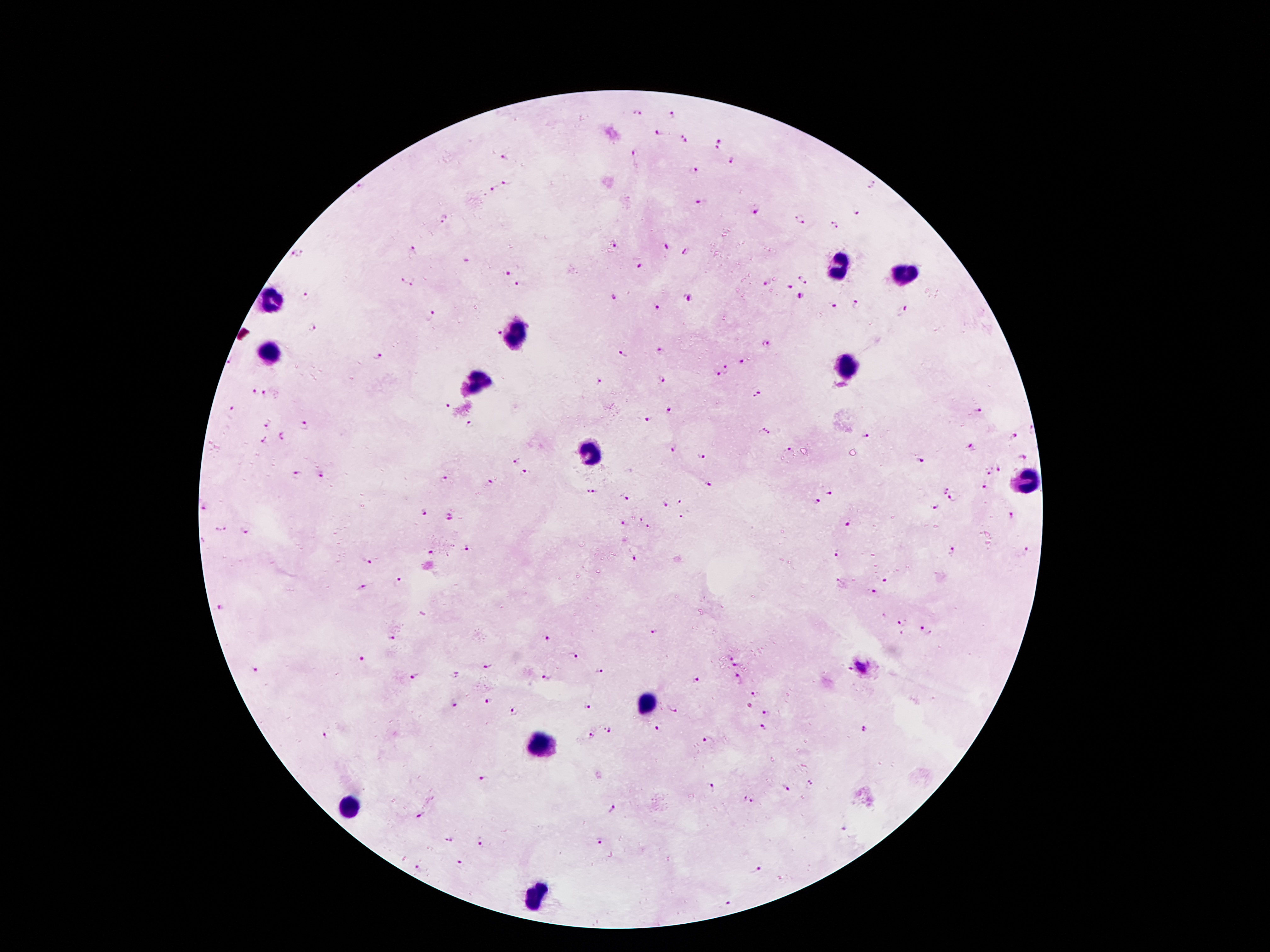 Giemsa stain. Thick blood film. Image is 1270×952 pixels. One field from this slide. Smartphone photograph taken through the microscope eyepiece. Patient malaria status: infected with Plasmodium falciparum. 100x magnification.